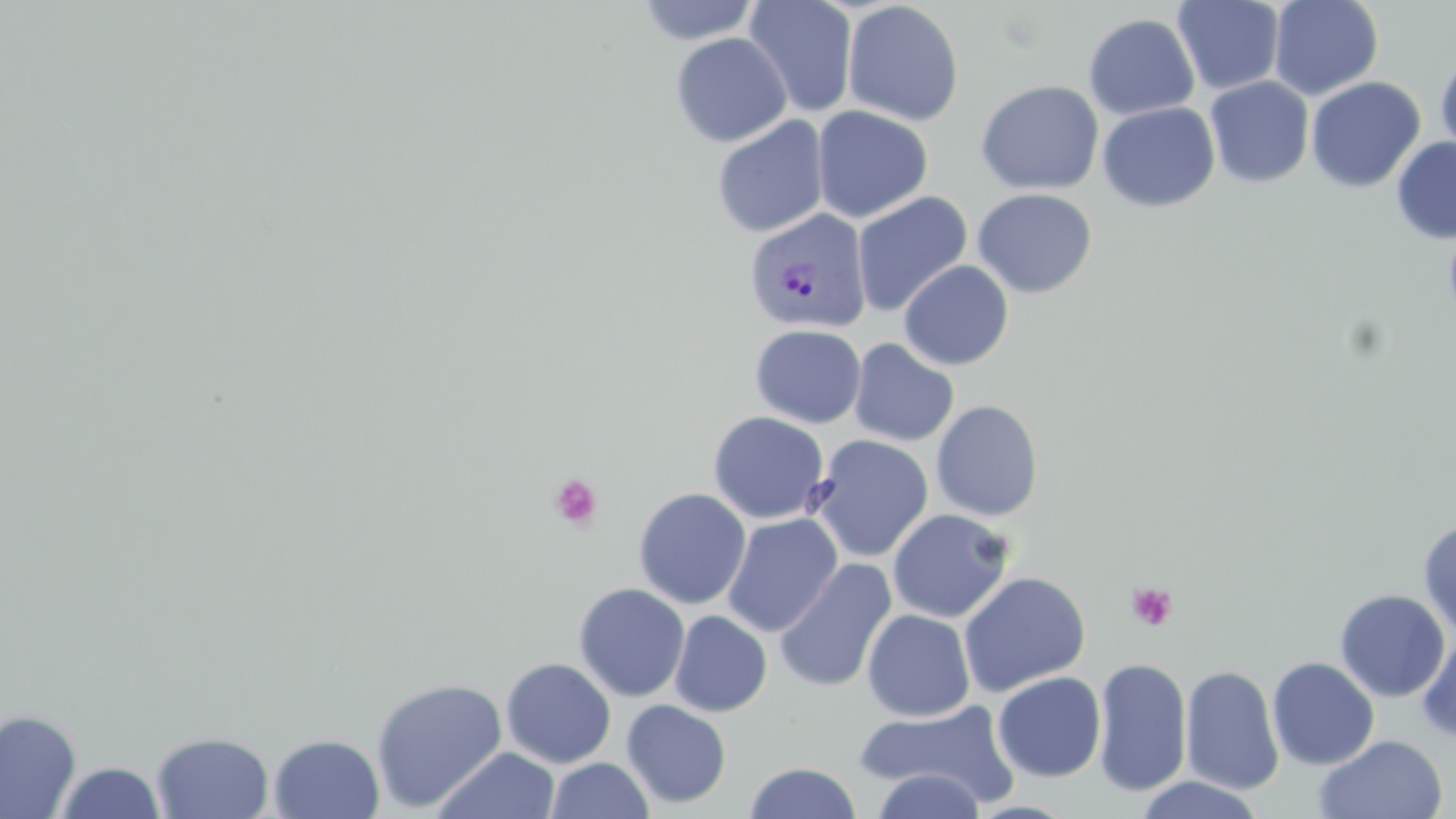

Summary:
  - Coordinate format: approximate bounding boxes as (x1, y1, x2, y2) in pixels
  - Platelet locations: (548, 472, 602, 531), (1127, 582, 1178, 630)
  - Plasmodium vivax-infected red blood cell locations: (743, 209, 872, 334)
  - Uninfected red blood cell locations: (635, 0, 761, 45), (743, 0, 858, 117), (1269, 0, 1383, 100), (1172, 1, 1286, 95), (842, 2, 964, 126), (1083, 13, 1200, 120), (670, 32, 792, 147), (1434, 52, 1456, 160), (1204, 76, 1314, 188), (1305, 77, 1426, 193), (975, 79, 1104, 195), (1097, 101, 1220, 212), (812, 105, 933, 223), (712, 115, 830, 238), (1391, 136, 1456, 244), (972, 188, 1098, 298), (851, 191, 973, 317), (1443, 218, 1456, 336), (898, 260, 1014, 371), (750, 324, 867, 429), (849, 338, 960, 447), (931, 399, 1044, 522), (707, 411, 830, 524), (808, 434, 933, 562), (632, 487, 752, 609), (887, 508, 1014, 623), (721, 512, 843, 637), (1418, 519, 1456, 638), (774, 558, 897, 693), (959, 571, 1091, 696), (573, 582, 690, 702), (1334, 589, 1450, 702), (862, 608, 975, 721), (669, 610, 772, 717), (1417, 633, 1456, 743), (1092, 656, 1192, 797), (501, 657, 616, 768), (1267, 657, 1379, 770), (1180, 665, 1285, 795), (992, 671, 1106, 782), (370, 677, 508, 812), (622, 699, 732, 809), (855, 700, 1020, 809), (0, 709, 81, 818), (151, 730, 274, 818), (268, 733, 385, 818), (1314, 733, 1448, 819), (430, 747, 559, 819), (544, 757, 654, 819), (54, 761, 167, 818), (744, 762, 862, 819), (873, 769, 985, 818), (1135, 775, 1264, 818)
  - Slide-level diagnosis: Plasmodium vivax
  - Image size: 1456×819 pixels
  - Modality: optical microscopy
  - Field of view: one of a larger specimen
  - Magnification: 1000x
  - Stain: May-Grünwald-Giemsa
  - Preparation: thin blood film